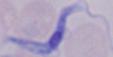

modality: micrograph
identification: trypanosome
magnification: 1000x